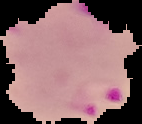 Result: Plasmodium parasites detected. The area outside the segmented cell region is set to black. From a thin blood film. Image is 142×124 pixels.